Identify the cell.
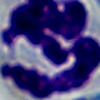

A leukocyte.

magnification = 1000x
modality = micrograph